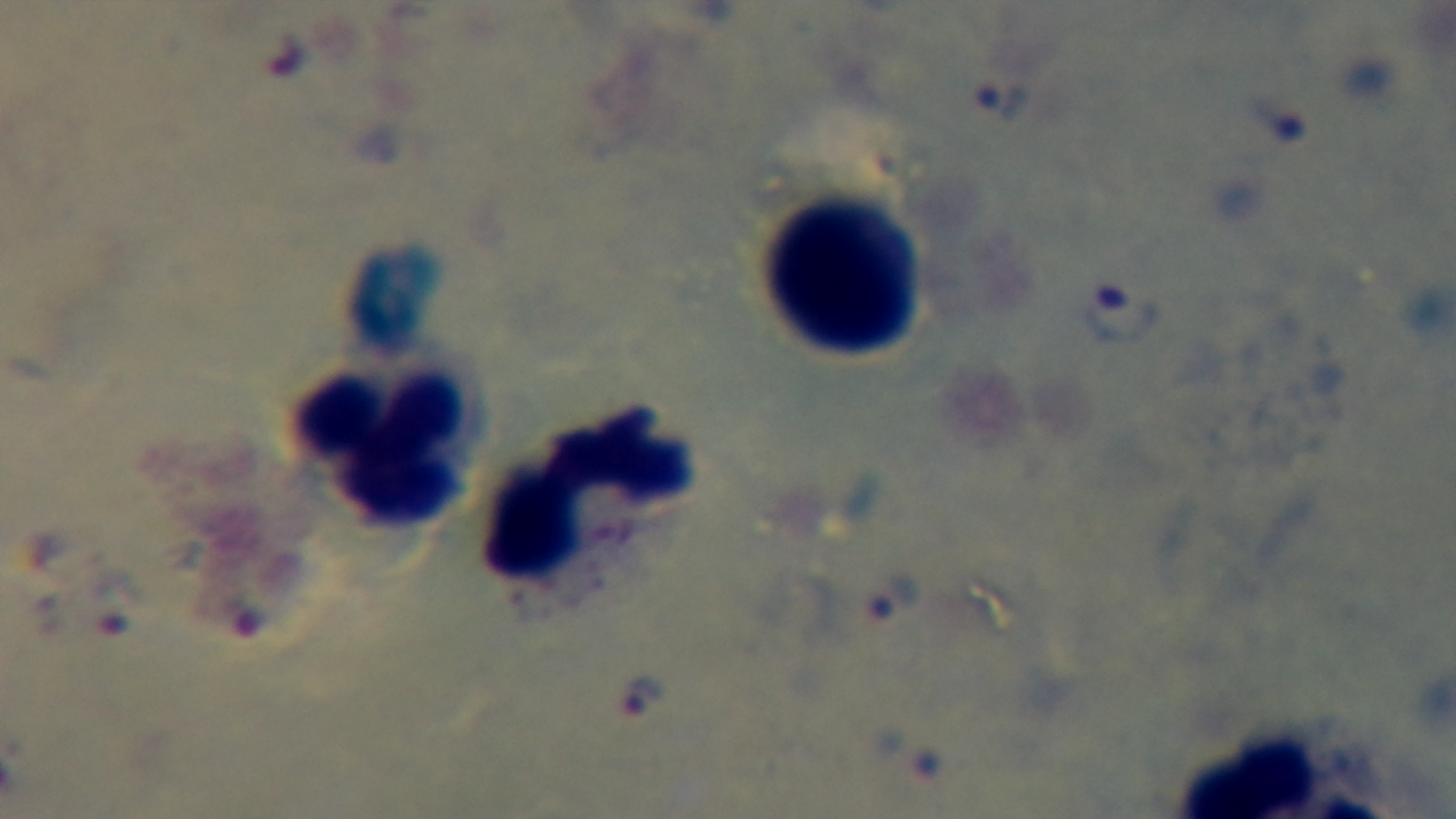 Malaria status: positive. Light microscopy. One field from the slide. 100x oil-immersion objective. Preparation: thick. Giemsa stain. Captured with a mounted 4K digital camera.